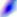
Summary:
  - Modality: micrograph
  - Magnification: 400x
  - Identification: Toxoplasma gondii